Comment on the morphology of the erythrocytes.
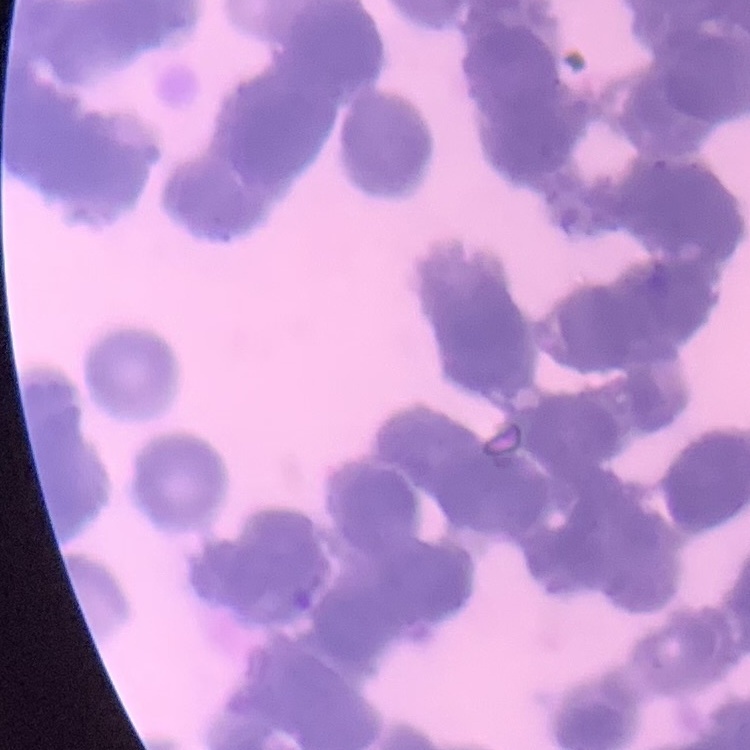

They show rouleaux formation.

preparation = thin blood smear
stain = Field's or Giemsa
image type = square crop of a larger photomicrograph